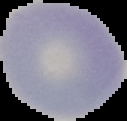
image_size: 127×121 pixels
preparation: thin blood smear
result: no malaria parasites seen
image_type: segmented cell region with the area outside set to black